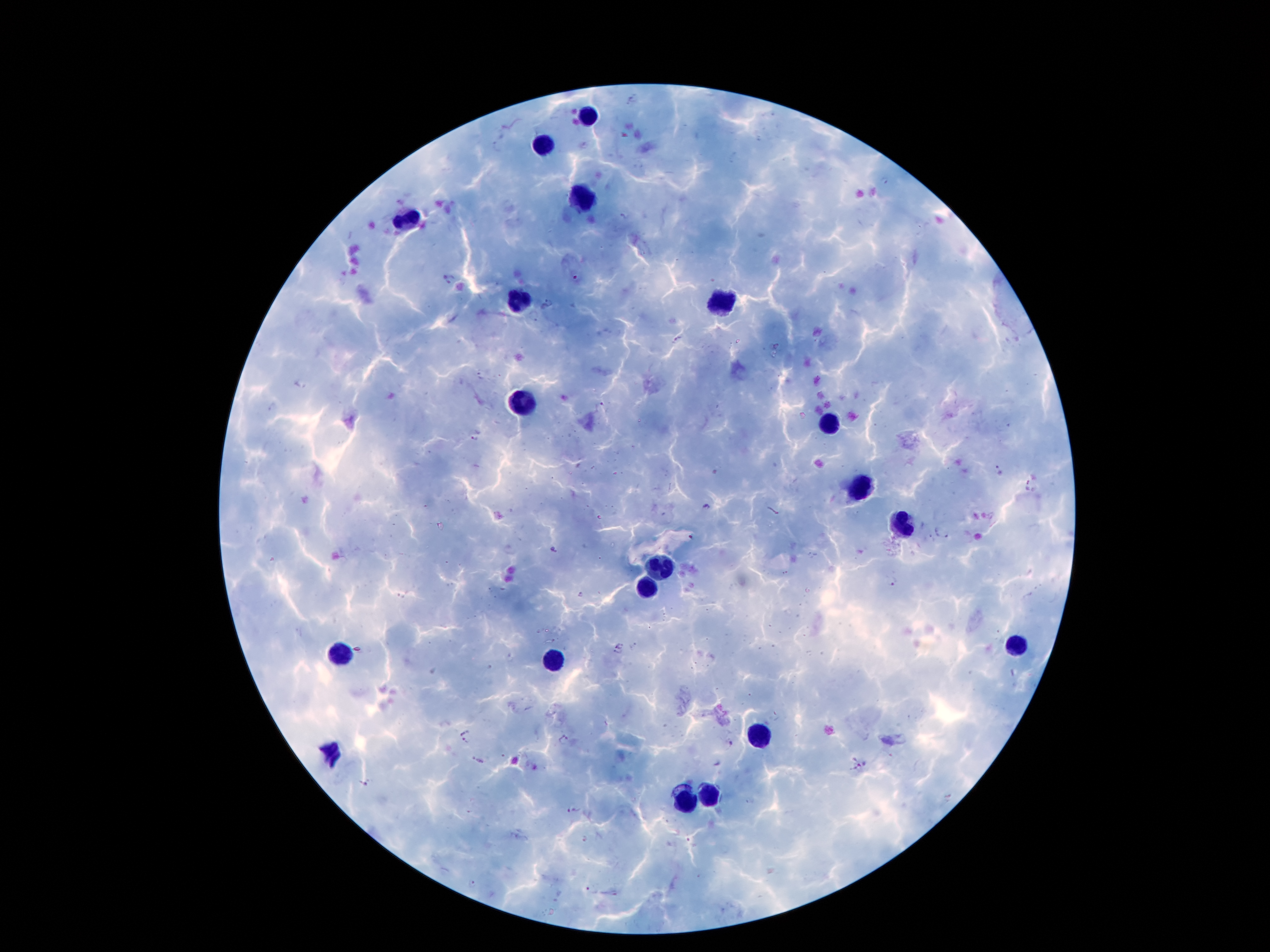

coordinate format = approximate object centers, in pixels from the top-left corner
leukocyte locations = (x=589, y=114), (x=544, y=144), (x=582, y=198), (x=408, y=220), (x=518, y=299), (x=720, y=300), (x=526, y=401), (x=830, y=422), (x=860, y=485), (x=903, y=524), (x=660, y=569), (x=647, y=588), (x=1017, y=646), (x=341, y=655), (x=554, y=662), (x=755, y=735), (x=330, y=752), (x=711, y=791), (x=686, y=800)
Plasmodium parasite locations = (x=633, y=99), (x=497, y=146), (x=623, y=216), (x=450, y=280), (x=549, y=304), (x=534, y=316), (x=676, y=341), (x=479, y=377), (x=299, y=383), (x=272, y=407), (x=602, y=409), (x=476, y=439), (x=998, y=471), (x=1033, y=485), (x=707, y=506), (x=943, y=533), (x=690, y=537), (x=555, y=550), (x=894, y=580), (x=579, y=595), (x=619, y=644), (x=635, y=646), (x=618, y=652), (x=464, y=729), (x=564, y=739), (x=464, y=740), (x=732, y=744), (x=476, y=761), (x=862, y=766), (x=363, y=785), (x=573, y=809), (x=585, y=840), (x=691, y=843), (x=472, y=883), (x=592, y=890)
image size = 1270×952 pixels
magnification = 100x
field of view = single
stain = Giemsa
capture = smartphone camera through the microscope eyepiece
patient malaria status = positive for Plasmodium falciparum
preparation = thick peripheral-blood smear